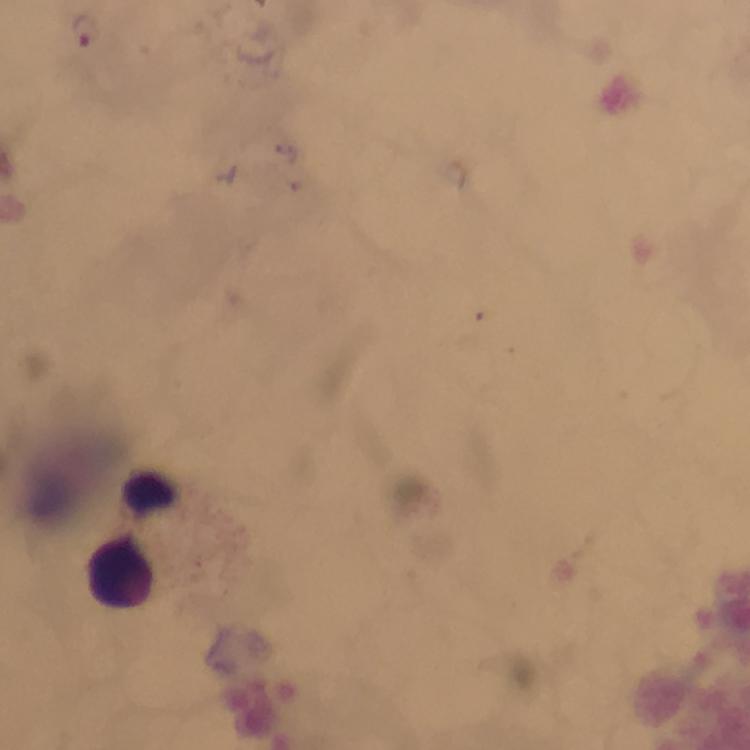

Approximate centers as [x, y] in pixels. Plasmodium parasite locations: [86, 30]. Leukocyte locations: [150, 494], [123, 569]. Photographed through the microscope with a smartphone camera. Thick blood film. Giemsa-stained preparation. From a malaria diagnostic workup. Image is 750×750 pixels. At 100x magnification. A crop from one field of view. Immersion oil was used.